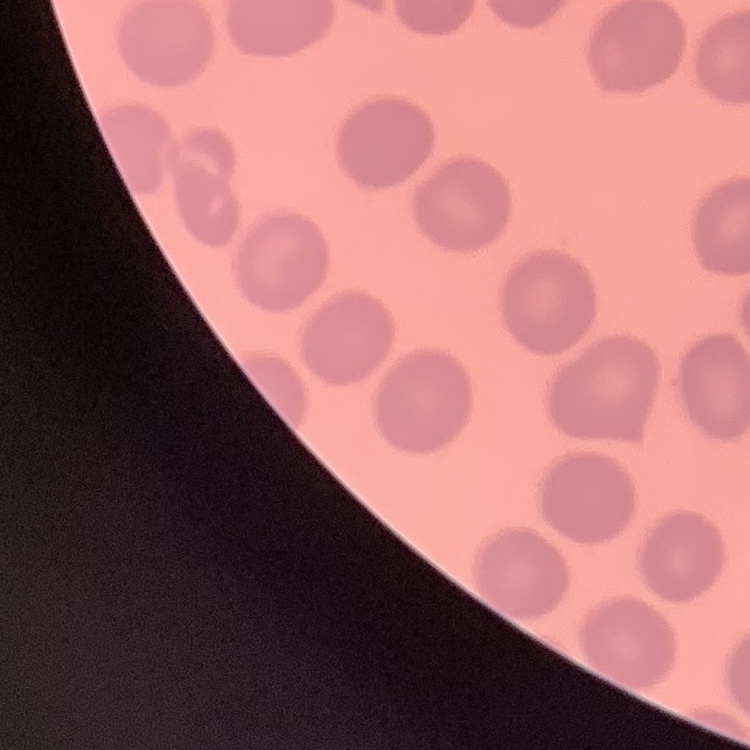

erythrocyte morphology = no rouleaux formation
preparation = thin blood smear
image type = square crop of a larger photomicrograph
stain = Field's or Giemsa